State which parasite is depicted.
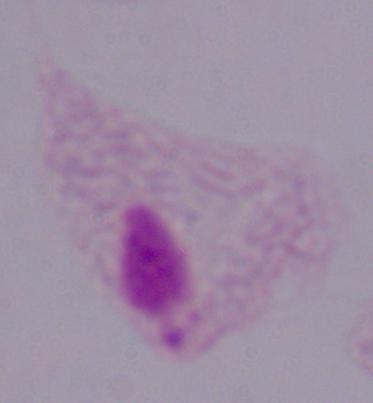

This is a trichomonad.

Captured at 1000x magnification. Micrograph.